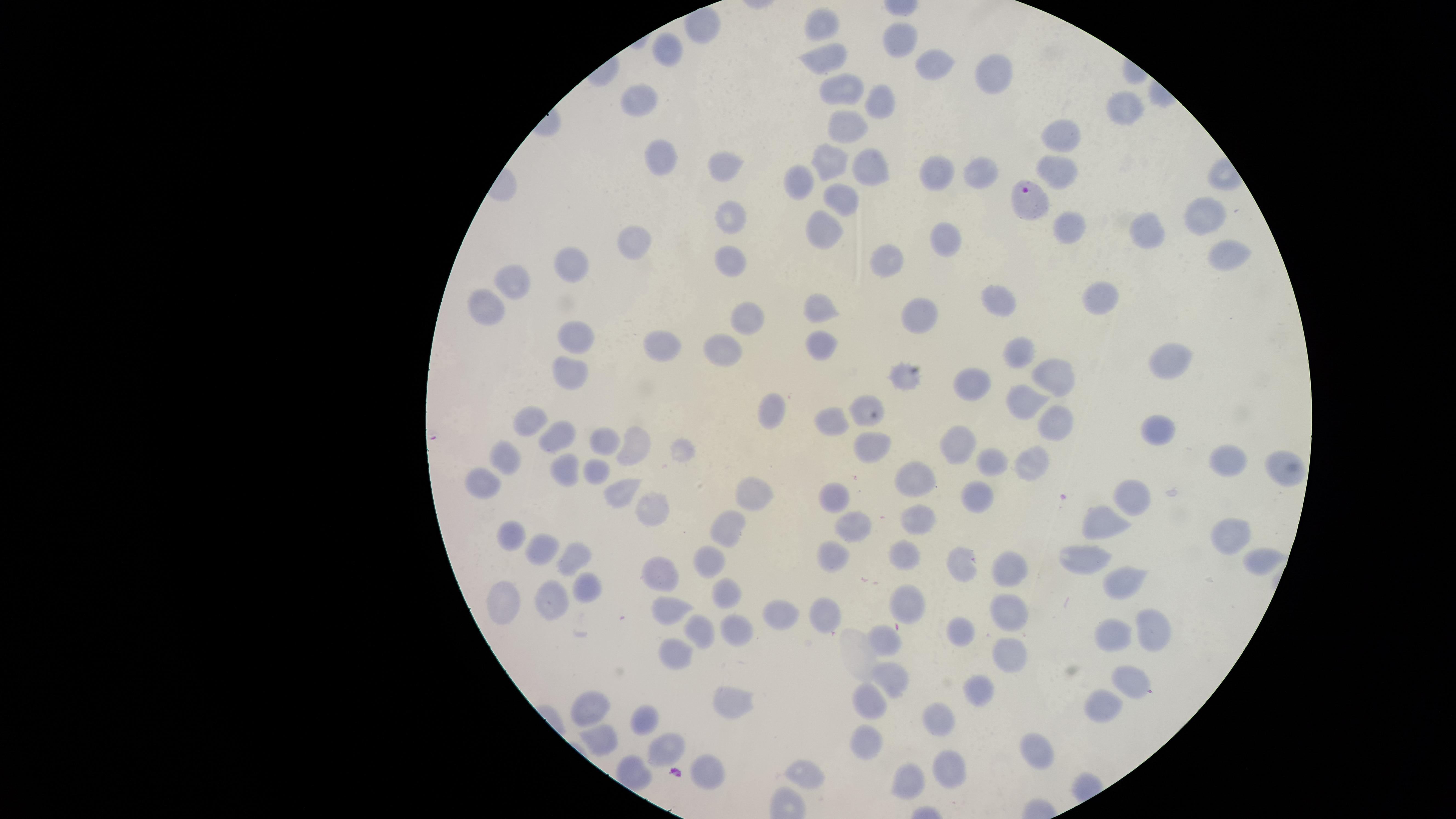
{
  "stain": "Giemsa",
  "capture": "smartphone photograph through the microscope eyepiece",
  "presence": "malaria parasites seen",
  "species": "Plasmodium falciparum",
  "visible_region": "circular",
  "field_of_view": "single",
  "uninfected_red_blood_cells": "approximate marker points as (x, y) in pixels: (823, 24), (897, 37), (668, 51), (821, 55), (934, 64), (996, 71), (843, 82), (641, 101), (881, 106), (1127, 106), (845, 129), (1062, 137), (664, 154), (832, 157), (720, 165), (876, 165), (981, 168), (1061, 170), (938, 171), (806, 178), (839, 195), (1203, 214), (733, 217), (1075, 224), (827, 226), (1153, 229), (948, 242), (636, 244), (1226, 256), (894, 260), (576, 264), (731, 264), (518, 280), (1107, 298), (1000, 301), (493, 305), (821, 308), (917, 315), (749, 320), (579, 339), (820, 344), (661, 345), (1015, 350), (726, 352), (1171, 361), (1058, 372), (573, 373), (902, 377), (977, 388), (1023, 399), (866, 403), (774, 409), (1051, 417), (533, 418), (829, 420), (1151, 430), (872, 441), (561, 442), (600, 442), (952, 442), (634, 444), (508, 457), (1232, 461), (997, 462), (1035, 462), (560, 469), (1280, 469), (592, 470), (484, 479), (917, 481), (621, 491), (759, 496), (1135, 496), (971, 500), (827, 504), (651, 510), (915, 522), (1105, 523), (727, 525), (850, 528), (508, 536), (1232, 536), (539, 552), (901, 552), (576, 556), (709, 559), (832, 559), (1083, 561), (963, 564), (1258, 564), (1006, 571), (664, 572), (1120, 582), (500, 592), (584, 593), (724, 593), (549, 603), (911, 603), (666, 604), (1004, 610), (778, 614), (824, 615), (1149, 626), (701, 629), (736, 632), (961, 634), (885, 641), (1114, 642), (675, 650), (1005, 657), (1136, 682), (887, 685), (981, 687), (728, 703), (866, 704), (1107, 706), (594, 710), (940, 718), (647, 719), (603, 739), (866, 746), (664, 749), (1041, 749), (944, 766), (806, 768), (706, 773), (911, 782)",
  "image_size": "1456×819 pixels",
  "preparation": "thin smear of blood",
  "parasitized_red_blood_cells": "approximate marker points as (x, y) in pixels: (1026, 197)"
}